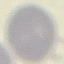

Summary:
  - Result: no malaria parasites detected
  - Capture: smartphone camera at the microscope eyepiece
  - Preparation: thin smear
  - Image type: cell patch, automatically extracted from a larger field of view and resized to 64 × 64 pixels
  - Stain: Giemsa